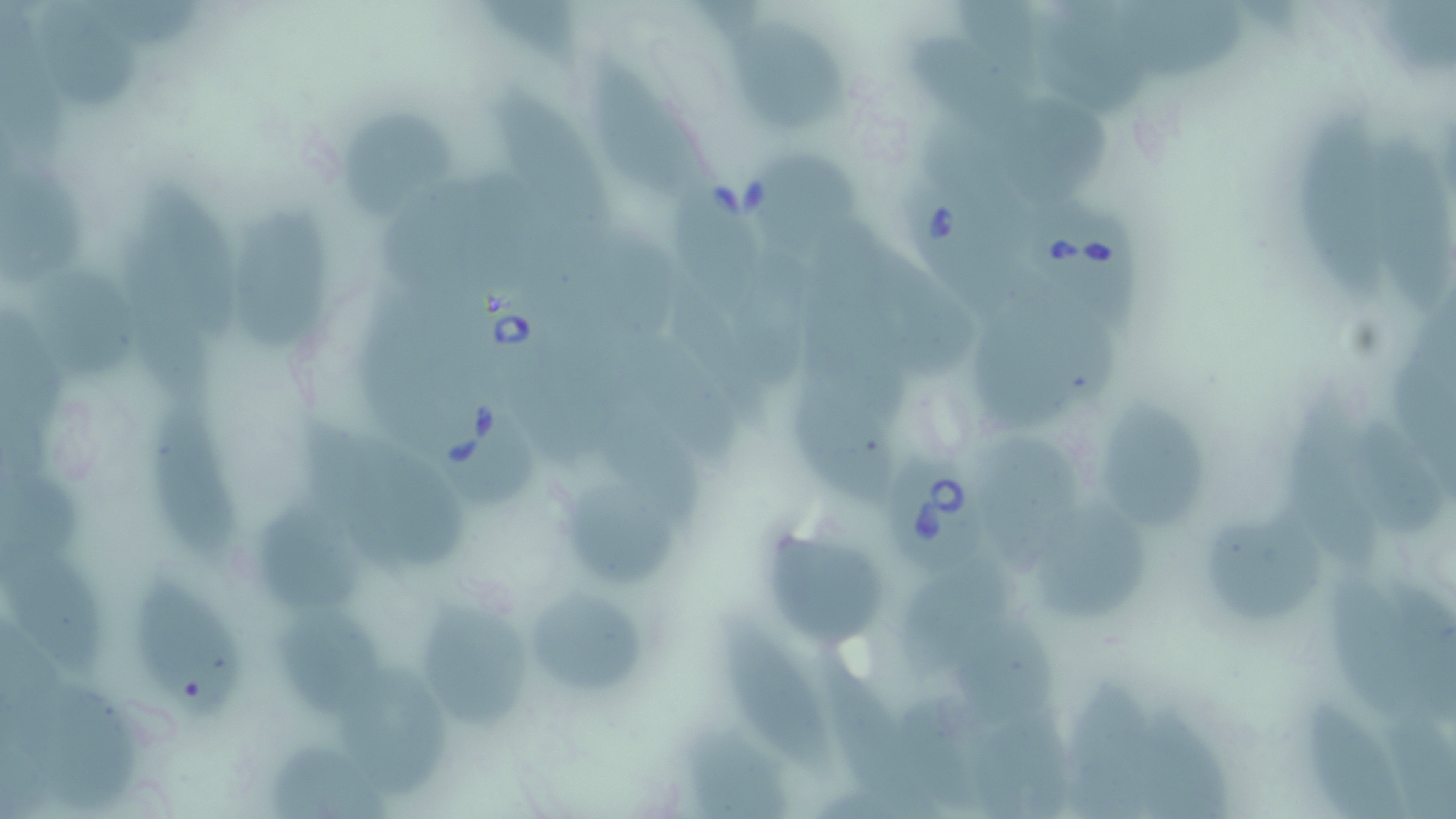

slide-level diagnosis = Babesia divergens
uninfected red blood cell locations = approximate bounding boxes as [x1, y1, x2, y2] in pixels: [33, 0, 140, 115], [1375, 0, 1456, 72], [1127, 1, 1247, 74], [1036, 9, 1156, 119], [734, 29, 852, 134], [908, 33, 1041, 150], [597, 63, 709, 203], [486, 88, 621, 234], [1005, 102, 1115, 203], [337, 105, 453, 217], [1292, 105, 1390, 310], [1373, 128, 1454, 315], [750, 151, 862, 258], [0, 168, 92, 286], [141, 183, 247, 341], [671, 187, 764, 307], [234, 208, 335, 353], [730, 252, 820, 393], [32, 269, 139, 381], [969, 313, 1089, 437], [797, 378, 900, 504], [1285, 391, 1389, 567], [1102, 401, 1209, 533], [153, 409, 244, 561], [303, 423, 467, 571], [979, 438, 1087, 577], [568, 479, 681, 592], [262, 503, 370, 618], [1040, 507, 1149, 620], [1206, 508, 1332, 630], [771, 526, 886, 647], [1, 537, 109, 682], [901, 570, 1019, 676], [1319, 572, 1428, 731], [138, 584, 245, 723], [532, 591, 647, 700], [419, 597, 534, 730], [277, 610, 385, 716], [951, 611, 1061, 720], [723, 615, 834, 779], [823, 653, 945, 819], [339, 668, 465, 796], [1064, 678, 1156, 819], [684, 723, 790, 819], [268, 743, 399, 819]
magnification = 1000x
preparation = thin blood smear
Babesia divergens-infected red blood cell locations = approximate bounding boxes as [x1, y1, x2, y2] in pixels: [898, 176, 1024, 321], [1029, 189, 1142, 336], [457, 285, 575, 409], [423, 375, 548, 510], [879, 446, 986, 578]
modality = light microscopy
field of view = one of a larger specimen
image size = 1456×819 pixels
stain = May-Grünwald-Giemsa